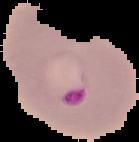

Summary:
  - Malaria status: parasitized
  - Image size: 139×142 pixels
  - Image type: segmented cell region with the area outside set to black
  - Preparation: thin blood film